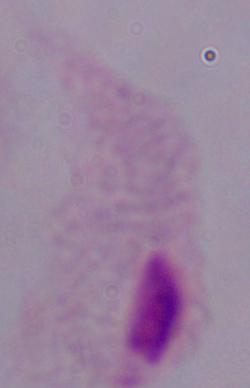
{
  "identification": "trichomonad",
  "magnification": "1000x",
  "modality": "photomicrograph"
}